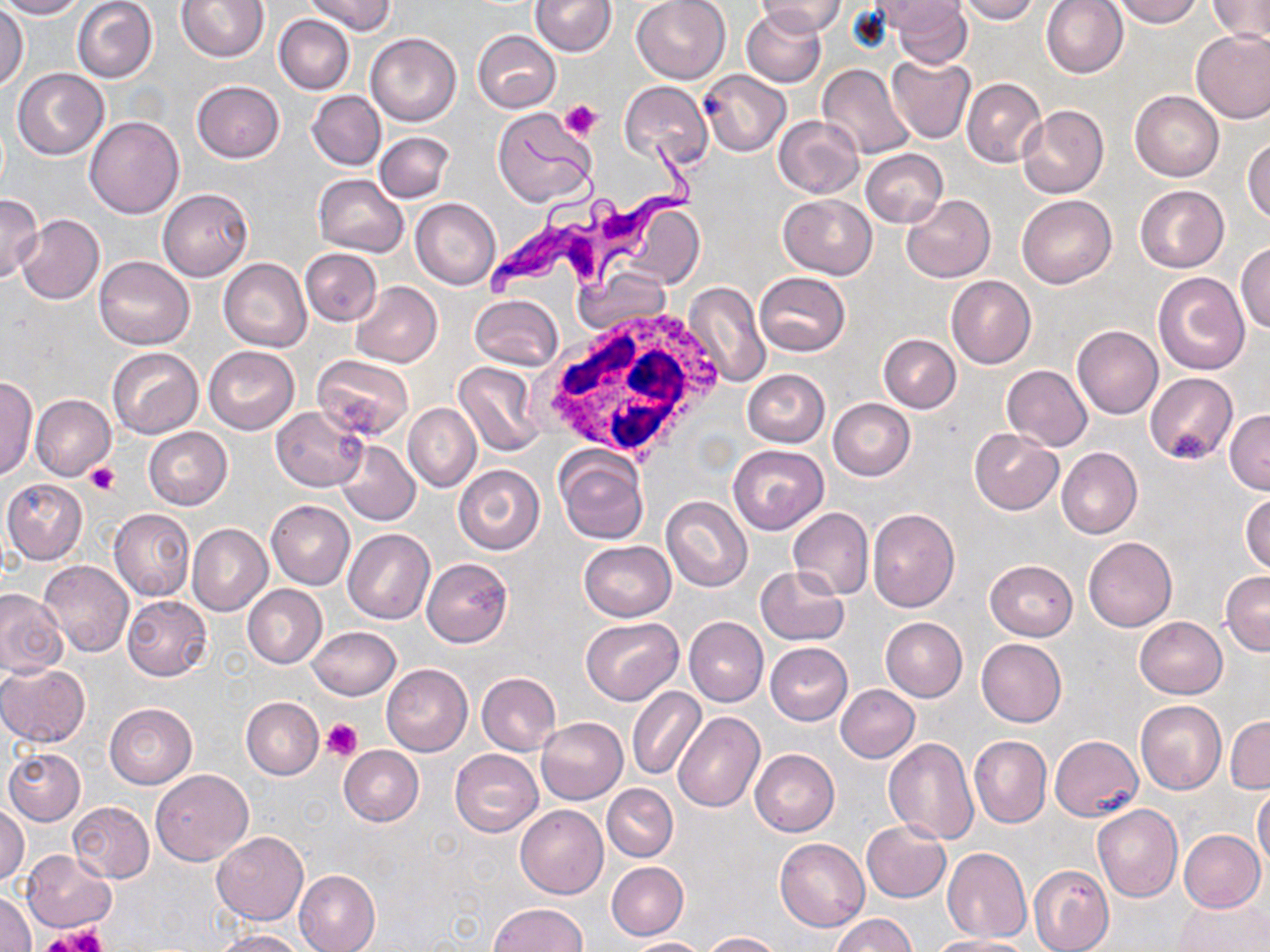

Approximate bounding boxes as named x1/y1/x2/y2 corners in pixels. Platelet locations: (x1=561, y1=100, x2=601, y2=139), (x1=84, y1=462, x2=119, y2=495), (x1=321, y1=719, x2=362, y2=760), (x1=52, y1=924, x2=109, y2=949). Uninfected red blood cell locations: (x1=0, y1=0, x2=86, y2=19), (x1=72, y1=0, x2=158, y2=83), (x1=176, y1=0, x2=269, y2=62), (x1=305, y1=0, x2=395, y2=36), (x1=530, y1=0, x2=616, y2=56), (x1=630, y1=0, x2=732, y2=83), (x1=754, y1=0, x2=845, y2=37), (x1=955, y1=0, x2=1039, y2=23), (x1=1041, y1=0, x2=1128, y2=78), (x1=1109, y1=0, x2=1202, y2=27), (x1=1206, y1=0, x2=1270, y2=42), (x1=870, y1=1, x2=964, y2=33), (x1=886, y1=1, x2=970, y2=67), (x1=0, y1=5, x2=28, y2=90), (x1=740, y1=8, x2=826, y2=88), (x1=275, y1=14, x2=354, y2=94), (x1=1191, y1=29, x2=1270, y2=123), (x1=473, y1=30, x2=560, y2=112), (x1=365, y1=33, x2=461, y2=126), (x1=886, y1=56, x2=977, y2=145), (x1=817, y1=64, x2=917, y2=162), (x1=12, y1=69, x2=108, y2=159), (x1=701, y1=70, x2=791, y2=156), (x1=962, y1=78, x2=1046, y2=167), (x1=192, y1=81, x2=285, y2=163), (x1=619, y1=82, x2=712, y2=167), (x1=307, y1=90, x2=386, y2=170), (x1=1131, y1=90, x2=1223, y2=182), (x1=1017, y1=105, x2=1107, y2=199), (x1=492, y1=107, x2=598, y2=208), (x1=772, y1=115, x2=862, y2=199), (x1=84, y1=116, x2=184, y2=219), (x1=374, y1=131, x2=454, y2=203), (x1=1244, y1=137, x2=1270, y2=224), (x1=861, y1=148, x2=947, y2=228), (x1=313, y1=174, x2=408, y2=257), (x1=1135, y1=185, x2=1229, y2=273), (x1=158, y1=188, x2=253, y2=280), (x1=0, y1=194, x2=44, y2=282), (x1=1016, y1=194, x2=1117, y2=289), (x1=779, y1=195, x2=876, y2=278), (x1=901, y1=195, x2=995, y2=284), (x1=410, y1=198, x2=501, y2=289), (x1=616, y1=204, x2=705, y2=291), (x1=15, y1=213, x2=105, y2=305), (x1=1235, y1=242, x2=1270, y2=336), (x1=299, y1=248, x2=382, y2=326), (x1=94, y1=255, x2=194, y2=350), (x1=219, y1=258, x2=310, y2=351), (x1=572, y1=267, x2=672, y2=334), (x1=755, y1=272, x2=850, y2=356), (x1=1153, y1=272, x2=1249, y2=375), (x1=946, y1=275, x2=1035, y2=369), (x1=683, y1=280, x2=771, y2=388), (x1=351, y1=281, x2=442, y2=367), (x1=469, y1=294, x2=564, y2=371), (x1=1072, y1=326, x2=1163, y2=418), (x1=879, y1=335, x2=960, y2=414), (x1=203, y1=346, x2=299, y2=435), (x1=105, y1=347, x2=202, y2=438), (x1=314, y1=355, x2=414, y2=440), (x1=454, y1=362, x2=542, y2=455), (x1=1001, y1=365, x2=1092, y2=451), (x1=742, y1=369, x2=830, y2=447), (x1=1146, y1=372, x2=1238, y2=464), (x1=0, y1=375, x2=37, y2=482), (x1=30, y1=394, x2=116, y2=481), (x1=828, y1=399, x2=915, y2=481), (x1=403, y1=403, x2=480, y2=493), (x1=270, y1=406, x2=369, y2=491), (x1=1225, y1=409, x2=1270, y2=494), (x1=143, y1=427, x2=232, y2=510), (x1=969, y1=428, x2=1064, y2=515), (x1=336, y1=441, x2=419, y2=526), (x1=729, y1=445, x2=827, y2=534), (x1=1057, y1=447, x2=1142, y2=539), (x1=554, y1=449, x2=648, y2=545), (x1=454, y1=465, x2=545, y2=555), (x1=2, y1=478, x2=88, y2=565), (x1=1241, y1=492, x2=1270, y2=576), (x1=661, y1=497, x2=753, y2=593), (x1=266, y1=500, x2=355, y2=589), (x1=787, y1=507, x2=873, y2=599), (x1=108, y1=508, x2=195, y2=602), (x1=867, y1=508, x2=960, y2=612), (x1=187, y1=524, x2=272, y2=616), (x1=343, y1=529, x2=435, y2=625), (x1=1084, y1=536, x2=1177, y2=631), (x1=579, y1=541, x2=676, y2=621), (x1=422, y1=557, x2=512, y2=646), (x1=986, y1=559, x2=1077, y2=641), (x1=39, y1=560, x2=133, y2=657), (x1=754, y1=566, x2=849, y2=646), (x1=1220, y1=571, x2=1270, y2=655), (x1=242, y1=585, x2=327, y2=668), (x1=0, y1=589, x2=67, y2=675), (x1=122, y1=595, x2=211, y2=680), (x1=1134, y1=616, x2=1227, y2=698), (x1=579, y1=617, x2=682, y2=705), (x1=683, y1=617, x2=768, y2=707), (x1=881, y1=617, x2=967, y2=701), (x1=308, y1=626, x2=400, y2=700), (x1=976, y1=638, x2=1066, y2=726), (x1=765, y1=642, x2=853, y2=724), (x1=381, y1=663, x2=473, y2=756), (x1=0, y1=664, x2=90, y2=747), (x1=476, y1=672, x2=561, y2=755), (x1=836, y1=685, x2=919, y2=763), (x1=627, y1=687, x2=706, y2=781), (x1=241, y1=697, x2=323, y2=780), (x1=1135, y1=700, x2=1226, y2=794), (x1=103, y1=702, x2=197, y2=789), (x1=673, y1=712, x2=766, y2=815), (x1=1226, y1=716, x2=1269, y2=793), (x1=536, y1=717, x2=628, y2=804), (x1=1049, y1=735, x2=1143, y2=821), (x1=883, y1=736, x2=979, y2=844), (x1=970, y1=736, x2=1052, y2=829), (x1=339, y1=746, x2=424, y2=826), (x1=3, y1=748, x2=84, y2=825), (x1=749, y1=749, x2=840, y2=836), (x1=450, y1=750, x2=542, y2=836), (x1=151, y1=769, x2=253, y2=865), (x1=602, y1=784, x2=678, y2=862), (x1=1253, y1=786, x2=1270, y2=870), (x1=68, y1=801, x2=154, y2=882), (x1=1, y1=804, x2=29, y2=886), (x1=515, y1=804, x2=608, y2=898), (x1=1092, y1=804, x2=1183, y2=903), (x1=861, y1=821, x2=951, y2=902), (x1=1178, y1=829, x2=1265, y2=913), (x1=212, y1=832, x2=308, y2=924), (x1=775, y1=838, x2=869, y2=931), (x1=943, y1=847, x2=1032, y2=943), (x1=22, y1=850, x2=117, y2=933), (x1=607, y1=862, x2=688, y2=939), (x1=1028, y1=864, x2=1115, y2=952), (x1=294, y1=869, x2=381, y2=952), (x1=1, y1=890, x2=36, y2=952), (x1=1175, y1=897, x2=1268, y2=952), (x1=487, y1=903, x2=586, y2=952), (x1=832, y1=914, x2=915, y2=952), (x1=211, y1=928, x2=308, y2=952), (x1=702, y1=931, x2=781, y2=951), (x1=928, y1=936, x2=1029, y2=952), (x1=626, y1=937, x2=707, y2=952). Trypanosoma brucei locations: (x1=486, y1=128, x2=712, y2=297). White blood cell locations: (x1=537, y1=305, x2=728, y2=461). Slide-level diagnosis: Trypanosoma brucei. May-Grünwald-Giemsa-stained preparation. Captured at 1000x magnification. One field of a larger specimen. Optical microscopy. Image is 1270×952 pixels. Thin blood smear.